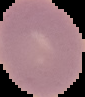
Image is 85×97 pixels. Malaria status: uninfected. The area outside the segmented cell region is set to black. From a thin blood smear.